Name the parasite shown.
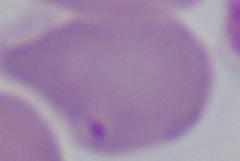
This is Babesia.

Photomicrograph. Captured at 1000x magnification.